Comment on the morphology of the red blood cells.
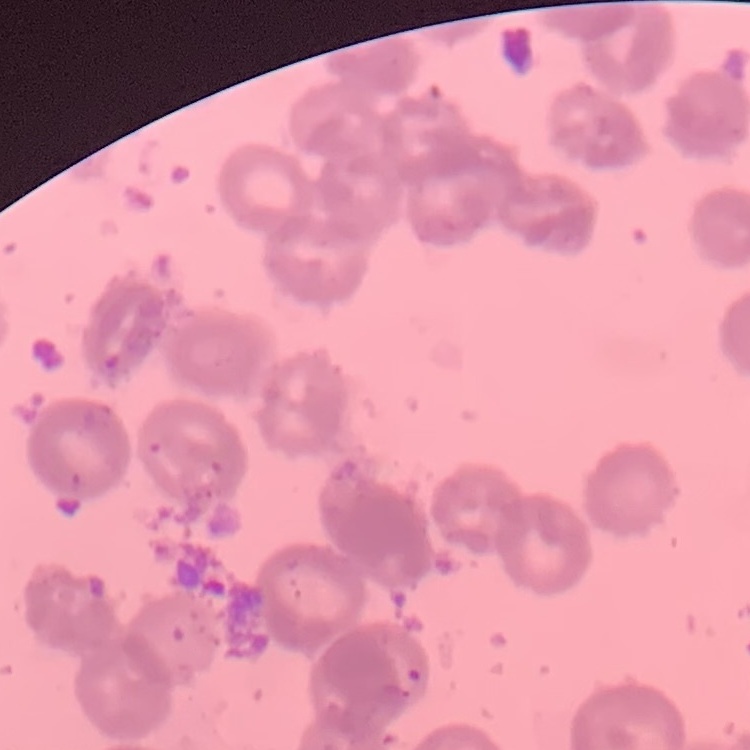

They show rouleaux formation.

Field's or Giemsa stain. One tile cut from a larger photomicrograph. Thin peripheral smear.